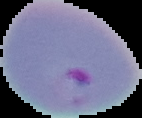

Summary:
  - Image size: 142×118 pixels
  - Image type: segmented cell region on a black background
  - Malaria status: parasitized
  - Preparation: thin blood film